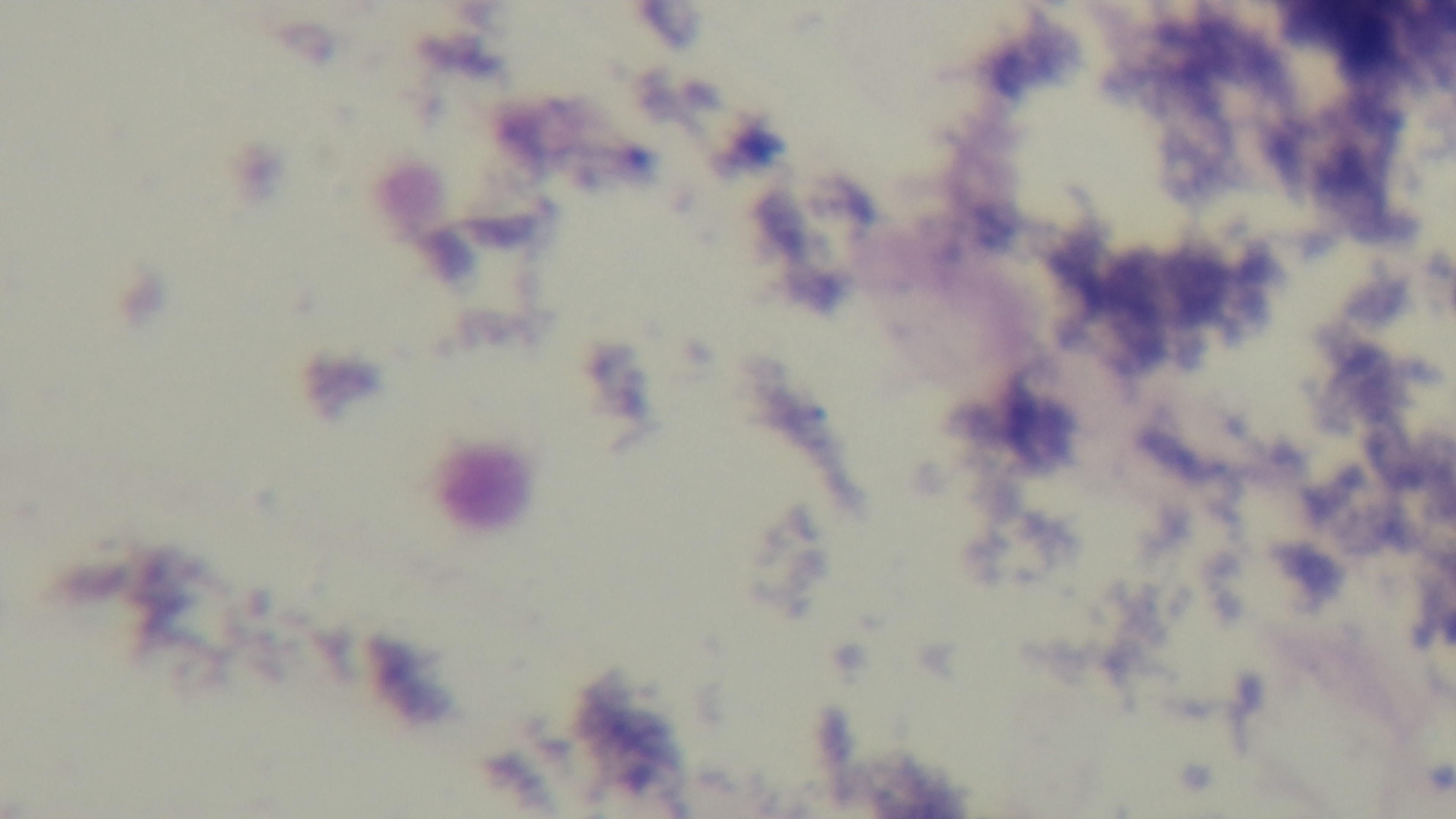

Summary:
  - Malaria status: uninfected
  - Objective: 100x oil immersion
  - Modality: light microscopy
  - Field of view: one from the slide
  - Stain: Giemsa
  - Capture: mounted 4K digital camera
  - Preparation: thick smear